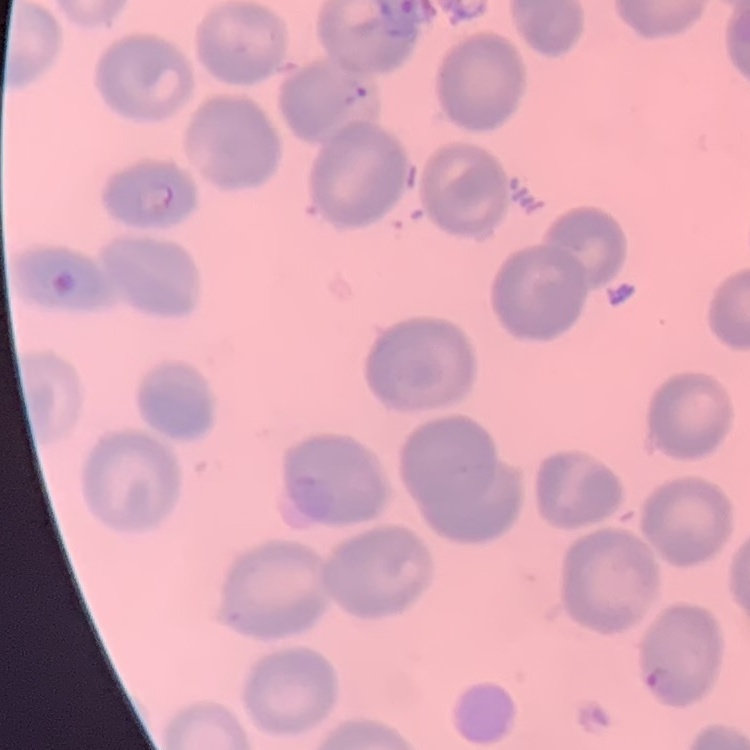
Summary:
  - Erythrocyte morphology: no rouleaux formation
  - Preparation: thin blood smear
  - Image type: one tile cut from a larger photomicrograph
  - Stain: Field's or Giemsa